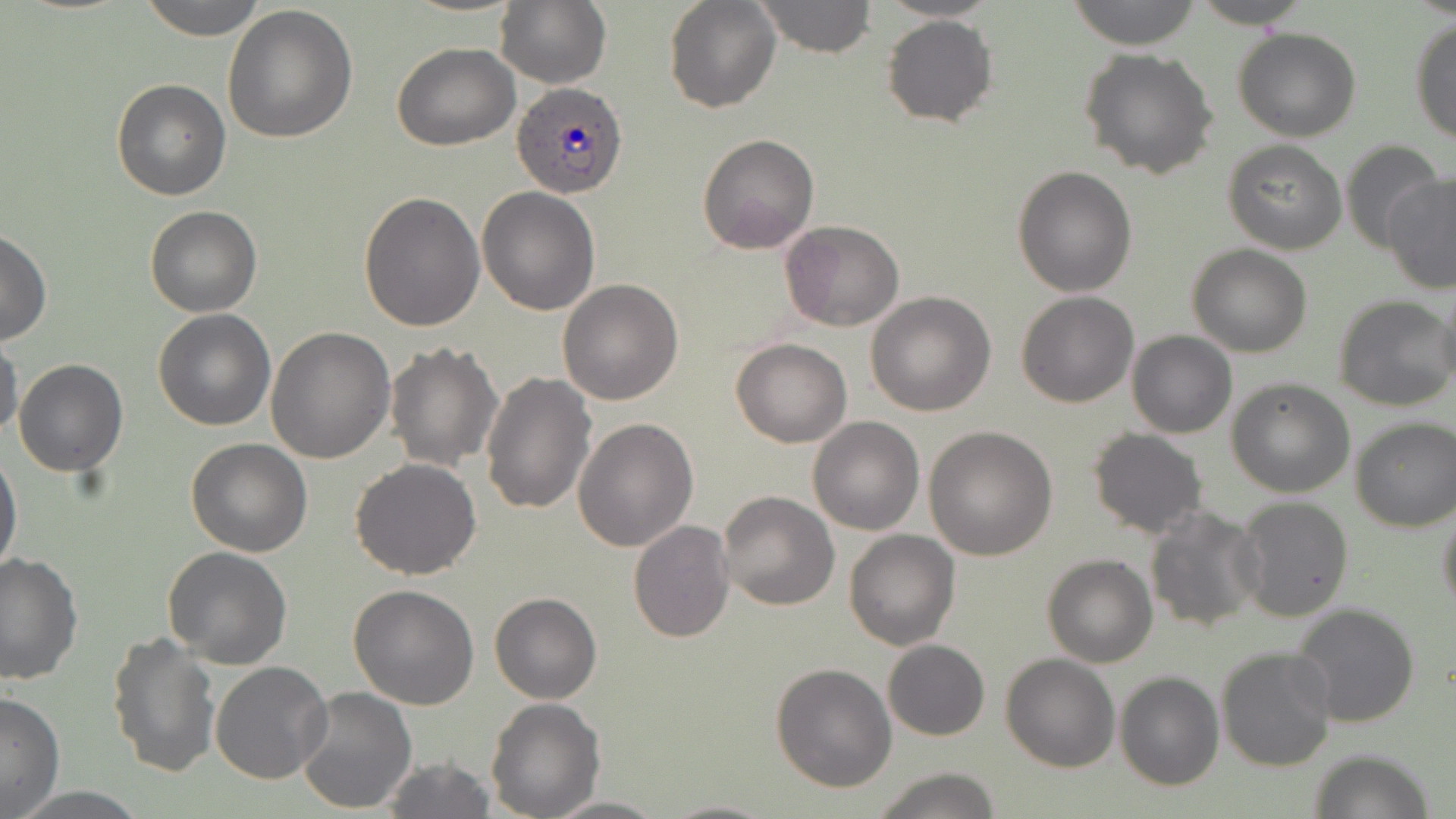
Approximate bounding boxes as [x1, y1, x2, y2] in pixels. Uninfected red blood cell locations: [139, 0, 270, 40], [496, 0, 611, 89], [663, 0, 781, 114], [755, 0, 875, 57], [873, 0, 1007, 23], [1067, 0, 1203, 50], [1189, 0, 1313, 28], [222, 4, 358, 143], [882, 15, 998, 127], [1408, 18, 1456, 145], [1233, 27, 1361, 143], [390, 42, 520, 149], [1078, 48, 1219, 179], [112, 79, 232, 201], [697, 134, 820, 255], [1222, 139, 1348, 255], [1340, 141, 1441, 253], [1012, 165, 1139, 297], [1381, 173, 1456, 294], [477, 187, 600, 315], [358, 192, 485, 331], [144, 206, 262, 317], [779, 219, 905, 332], [0, 229, 51, 346], [1186, 244, 1312, 358], [557, 279, 684, 405], [1434, 286, 1456, 395], [865, 291, 996, 416], [1015, 291, 1141, 407], [1333, 293, 1456, 410], [151, 308, 276, 430], [267, 327, 396, 465], [1126, 330, 1237, 439], [1, 332, 23, 441], [731, 337, 853, 447], [386, 342, 504, 471], [13, 358, 127, 475], [481, 370, 597, 514], [1227, 378, 1355, 497], [808, 415, 924, 535], [573, 418, 698, 551], [1350, 419, 1456, 531], [924, 425, 1058, 559], [1086, 428, 1208, 538], [185, 436, 312, 556], [1, 447, 23, 581], [350, 457, 481, 580], [715, 490, 839, 611], [1234, 495, 1353, 621], [1436, 501, 1456, 617], [1143, 505, 1265, 634], [627, 519, 735, 642], [844, 528, 960, 651], [162, 545, 292, 668], [1, 552, 82, 685], [1042, 554, 1157, 668], [349, 584, 480, 710], [489, 592, 601, 705], [1289, 602, 1422, 729], [106, 631, 220, 776], [882, 639, 989, 740], [1215, 645, 1337, 772], [1000, 653, 1121, 772], [209, 662, 331, 785], [770, 662, 898, 792], [1115, 671, 1224, 791], [297, 688, 417, 813], [0, 691, 65, 816], [485, 698, 604, 819], [1309, 747, 1436, 819], [378, 757, 497, 818], [870, 766, 1003, 819], [544, 794, 667, 817], [659, 798, 781, 818]. Plasmodium ovale-infected red blood cell locations: [511, 79, 626, 197]. Slide-level diagnosis: Plasmodium ovale. May-Grünwald-Giemsa stain. Light microscopy. Captured at 1000x magnification. Thin blood film. Image is 1456×819 pixels. Single field of view.